Describe the morphology of the red blood cells.
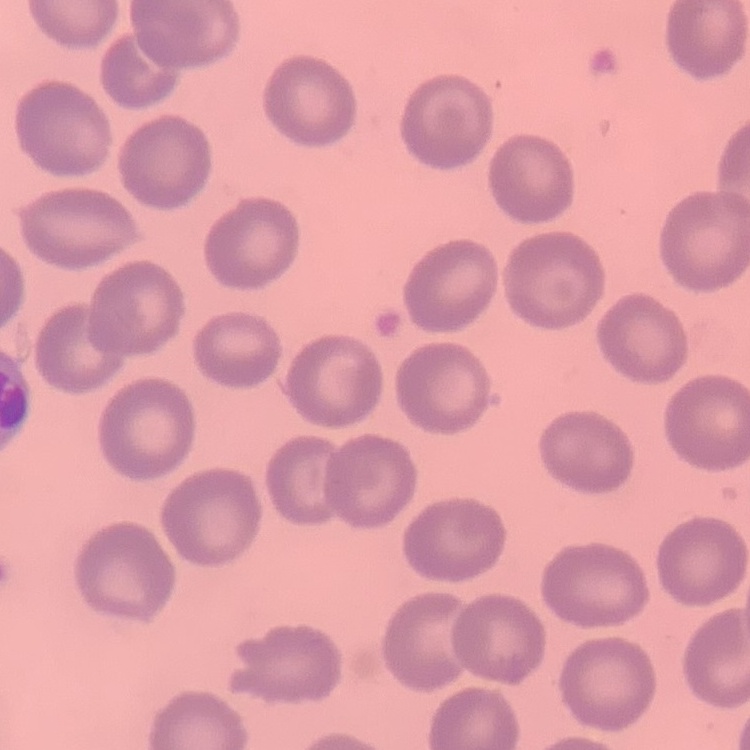
They show no rouleaux formation.

Thin blood film. One tile cut from a larger photomicrograph. Stained with either Field's or Giemsa.